Assess this cell for malaria.
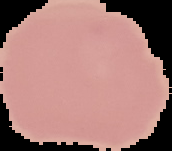

Uninfected.

From a thin blood smear. Segmented cell region on a black background. Image is 172×151 pixels.